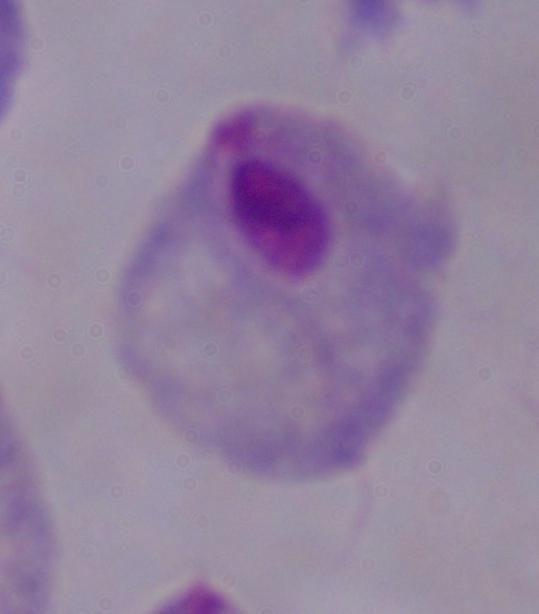

Summary:
  - Identification: trichomonad
  - Modality: micrograph
  - Magnification: 1000x